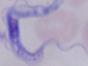

Summary:
  - Modality: micrograph
  - Identification: trypanosome
  - Magnification: 1000x